State which parasite is depicted.
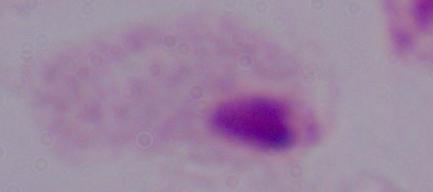

A trichomonad.

modality: micrograph
magnification: 1000x